Classify this cell by malaria status.
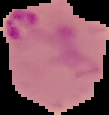
Parasitized.

image size = 109×115 pixels
preparation = thin blood film
image type = segmented cell region on a black background